Give the position of every Plasmodium parasite.
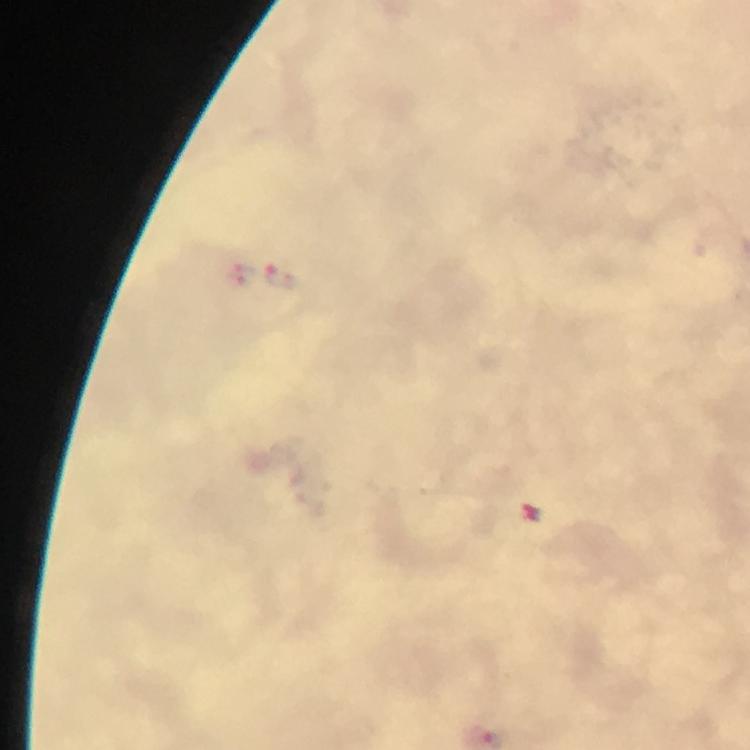

Approximate centers as (x, y) in pixels.
Plasmodium parasites: (280, 278).

From a malaria diagnostic workup. Photographed through the microscope with a smartphone camera. Giemsa stain. 100x magnification. Immersion oil applied. Thick blood film. Image is 750×750 pixels. Cropped region of a single field of view.